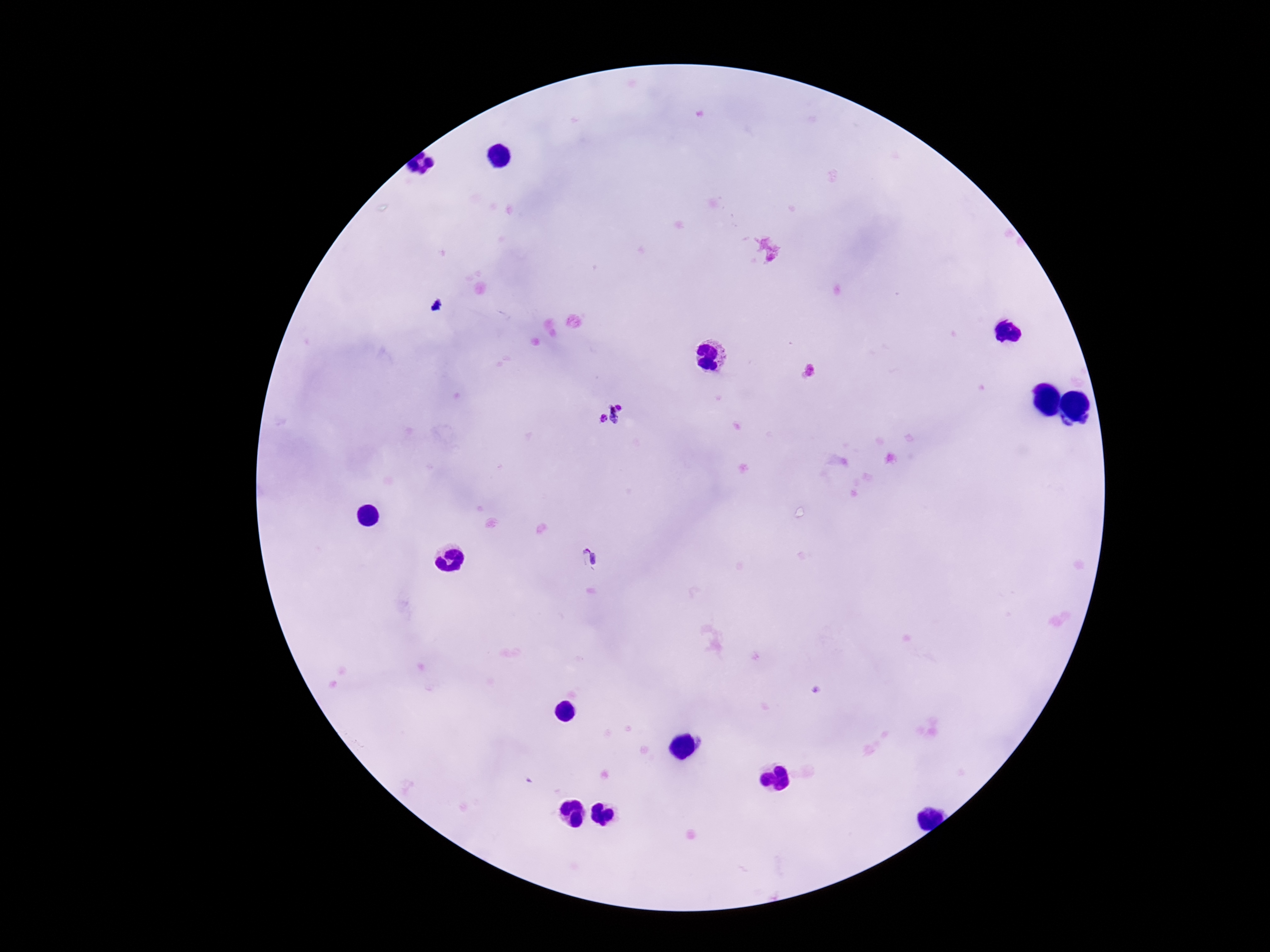

Approximate centers as (x, y) in pixels.
Summary:
  - Plasmodium parasite locations: (620, 407), (614, 415), (602, 418), (589, 558)
  - Field of view: one from this slide
  - Patient malaria status: positive
  - Image size: 1270×952 pixels
  - Preparation: thick blood smear
  - Capture: smartphone camera through the microscope eyepiece
  - Stain: Giemsa
  - Magnification: 100x